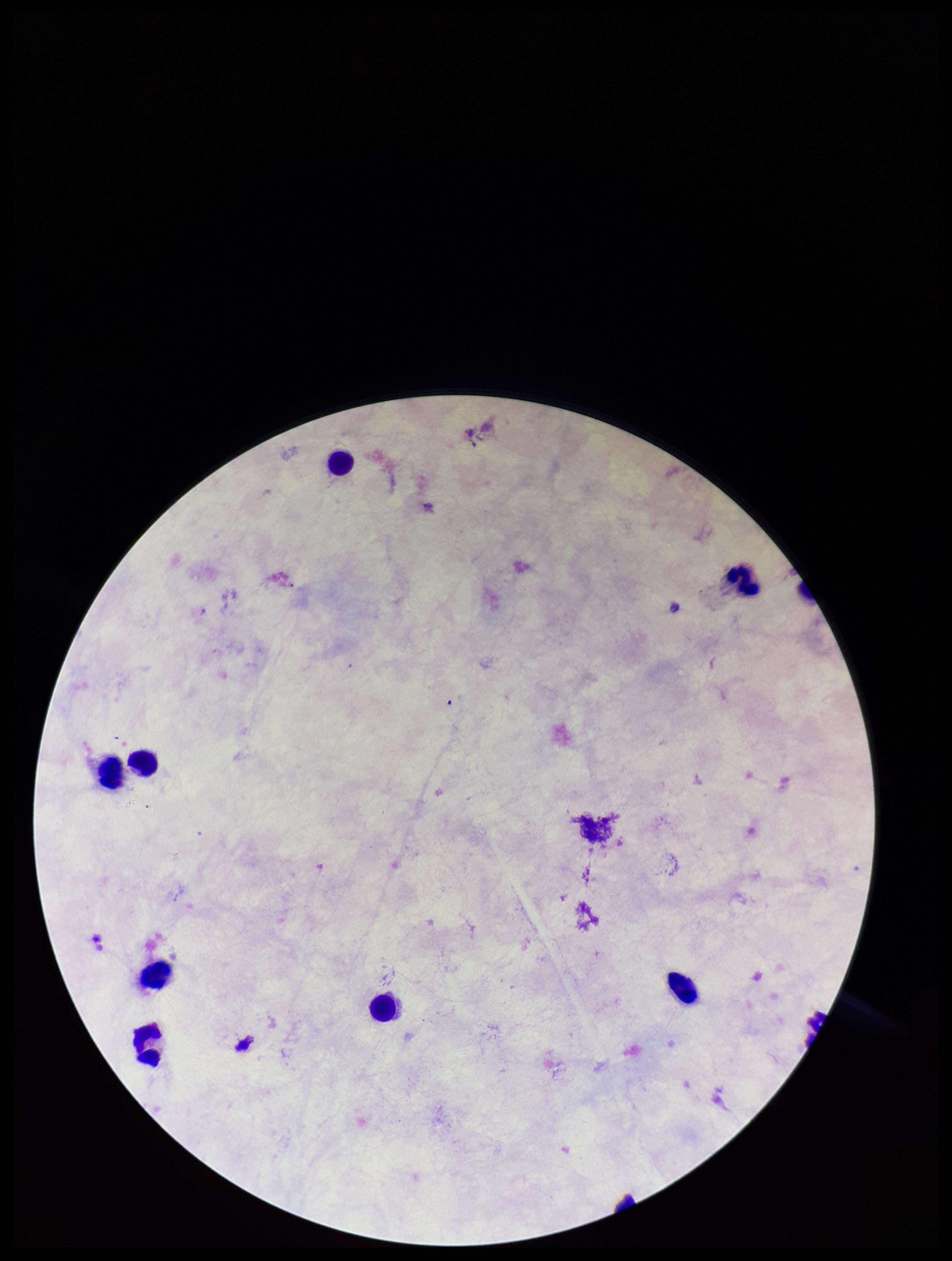 Parasite count: 0. Leukocyte count: 8. Single field of view. Giemsa stain. Patient malaria status: negative. Smartphone photograph taken through the eyepiece of a microscope. Plasmodium parasites: none identified. Image is 952×1261 pixels. Preparation: thick.